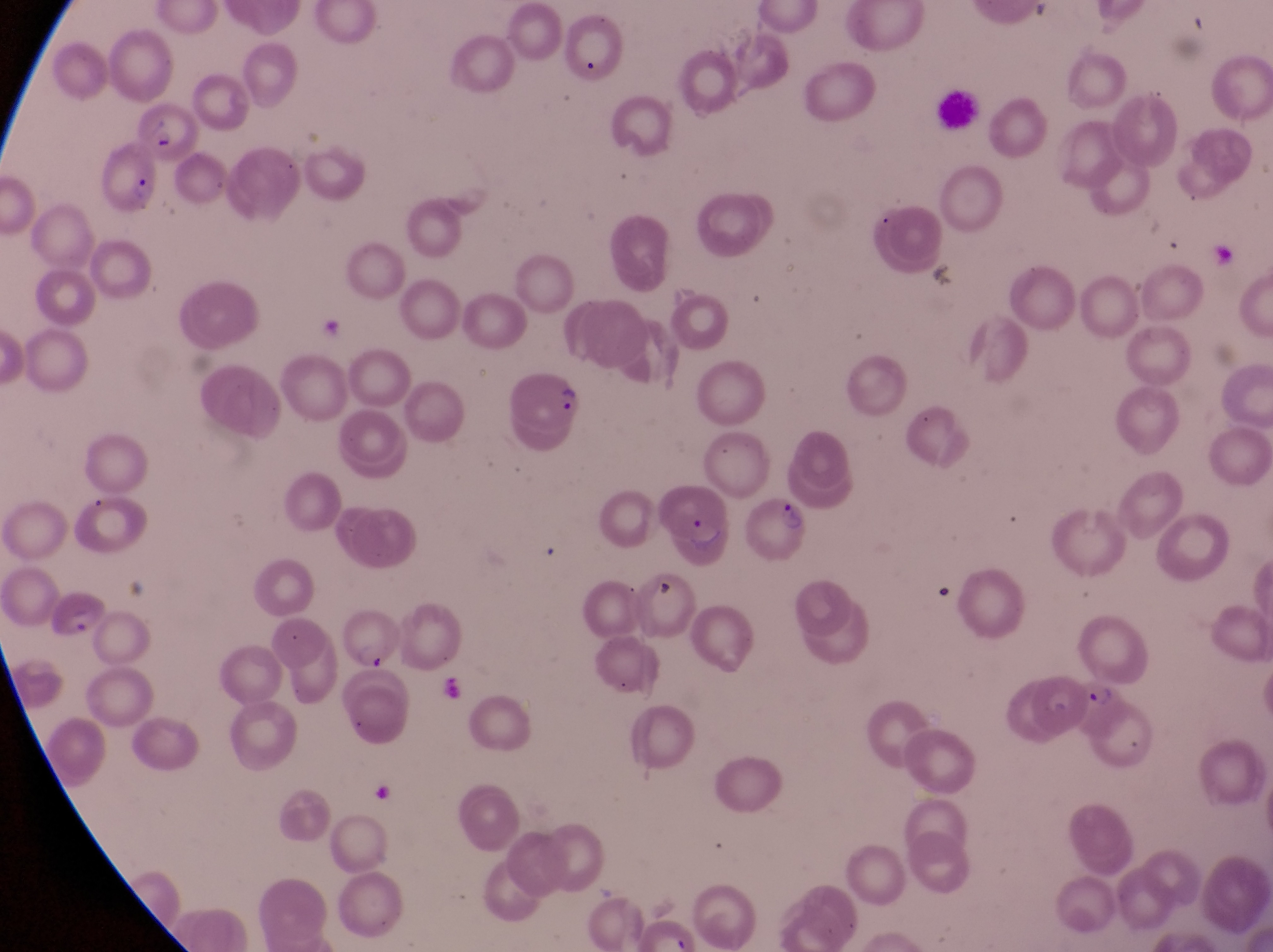
Approximate bounding boxes as {left, top, right, bottom} in pixels.
Summary:
  - Leukocyte locations: {934, 86, 985, 132}
  - Parasitised red blood cell locations: {135, 98, 197, 160}, {100, 143, 160, 220}, {502, 367, 590, 437}, {654, 474, 734, 569}, {749, 485, 804, 563}, {337, 616, 400, 674}, {1078, 681, 1133, 755}
  - Artifact (platelet-like body, stain precipitate, or debris) locations: {647, 579, 680, 611}, {369, 782, 399, 819}
  - Preparation: thin blood smear
  - Country: Uganda
  - Magnification: 1000x
  - Image size: 1273×952 pixels
  - Field of view: single
  - Capture: smartphone photograph through the eyepiece of an Olympus CX-23 microscope